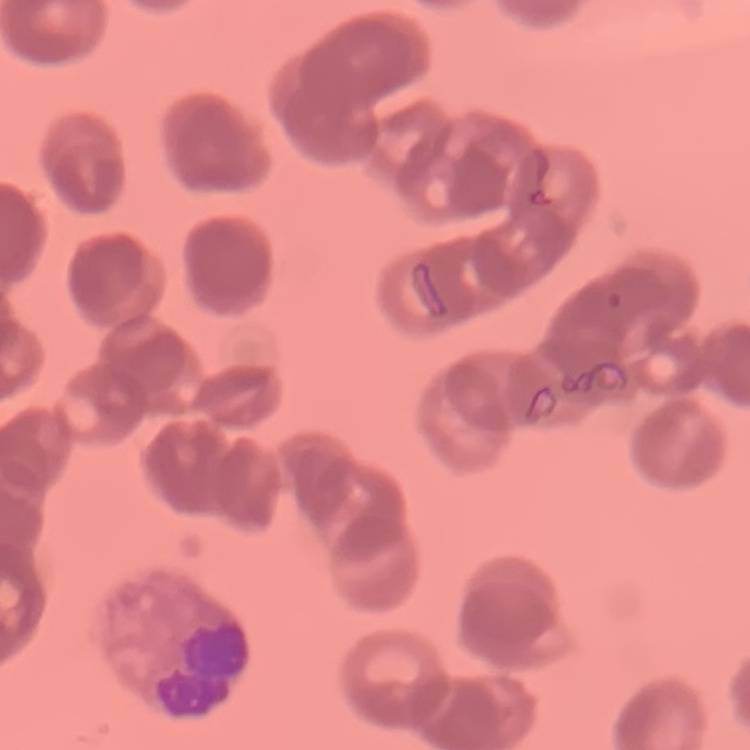

{
  "red_blood_cell_morphology": "rouleaux formation",
  "preparation": "thin blood smear",
  "stain": "Field's or Giemsa",
  "image_type": "square crop of a larger photomicrograph"
}